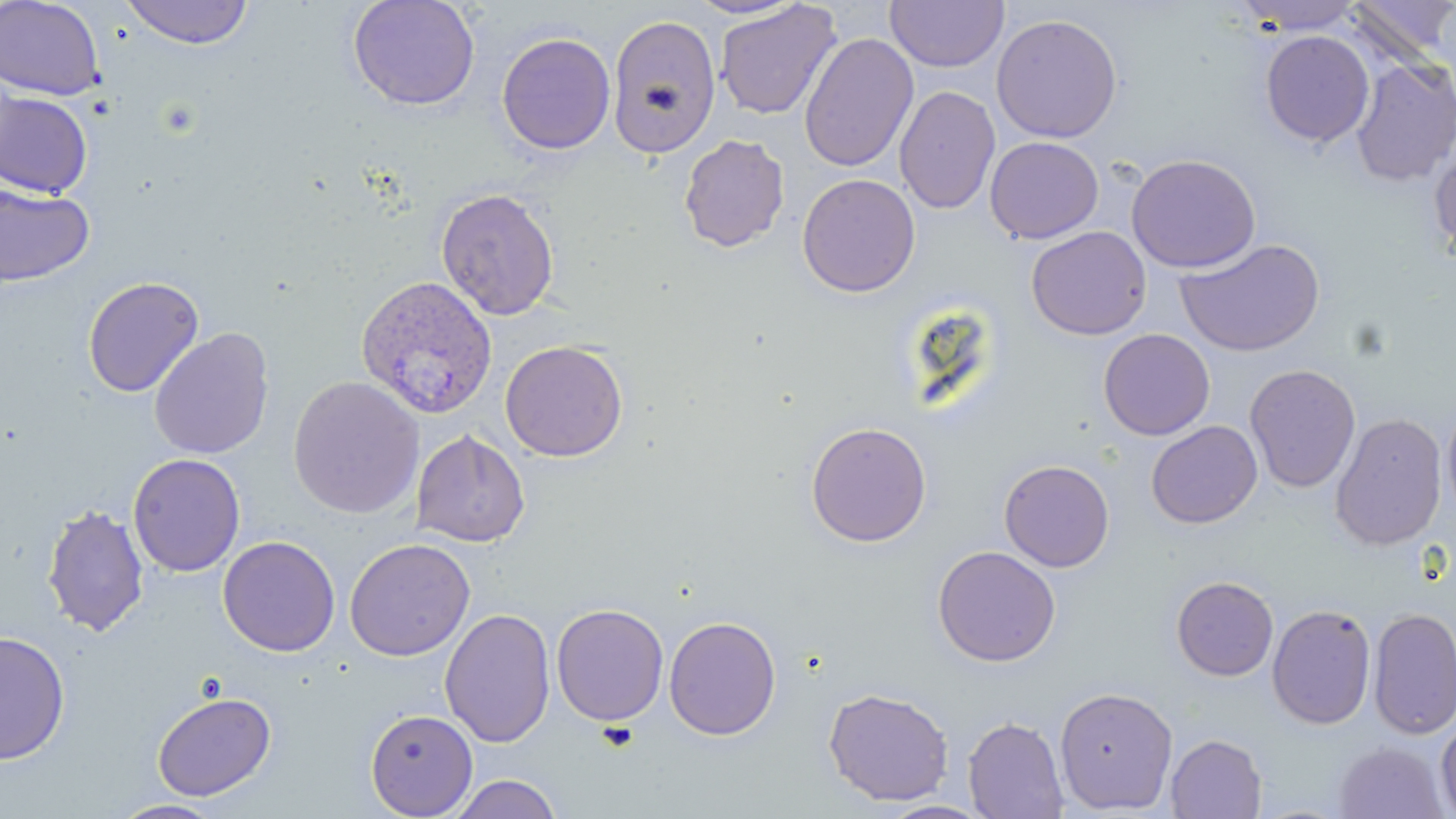

slide_level_diagnosis: Plasmodium ovale
image_size: 1456×819 pixels
stain: May-Grünwald-Giemsa
uninfected_red_blood_cell_locations: 'approximate bounding boxes as [x1, y1, x2, y2] in pixels: [0, 0, 107, 101], [120, 0, 254, 48], [346, 0, 481, 112], [683, 0, 807, 20], [1235, 0, 1365, 35], [1348, 0, 1455, 67], [713, 1, 842, 120], [885, 1, 1008, 72], [606, 13, 722, 159], [990, 13, 1123, 144], [1260, 30, 1374, 147], [496, 31, 616, 156], [798, 32, 919, 173], [1350, 57, 1456, 188], [894, 86, 1000, 215], [0, 91, 93, 199], [677, 134, 790, 253], [984, 136, 1104, 244], [1429, 141, 1456, 263], [1126, 153, 1261, 273], [796, 173, 921, 298], [0, 182, 95, 288], [435, 186, 561, 321], [1026, 225, 1152, 340], [1175, 238, 1326, 357], [83, 276, 204, 397], [148, 326, 275, 460], [1098, 328, 1216, 440], [500, 340, 629, 462], [1244, 363, 1361, 494], [288, 375, 425, 519], [1441, 398, 1456, 525], [1329, 412, 1447, 551], [1145, 420, 1263, 528], [804, 421, 933, 547], [411, 429, 530, 547], [127, 453, 246, 577], [998, 459, 1115, 572], [41, 503, 149, 637], [217, 535, 341, 656], [343, 538, 476, 662], [931, 545, 1062, 667], [1170, 575, 1279, 682], [551, 604, 669, 726], [1266, 604, 1377, 729], [1368, 607, 1456, 740], [440, 608, 556, 748], [663, 615, 782, 740], [0, 629, 71, 766], [1053, 685, 1179, 814], [822, 686, 955, 806], [151, 690, 277, 802], [364, 708, 478, 818], [962, 716, 1069, 819], [1436, 716, 1456, 817], [1165, 734, 1267, 818], [1333, 741, 1450, 819], [447, 773, 563, 819], [109, 799, 229, 818], [875, 799, 996, 818]'
plasmodium_ovale_infected_red_blood_cell_locations: 'approximate bounding boxes as [x1, y1, x2, y2] in pixels: [355, 275, 497, 419]'
modality: optical microscopy
preparation: thin blood film
field_of_view: single
magnification: 1000x